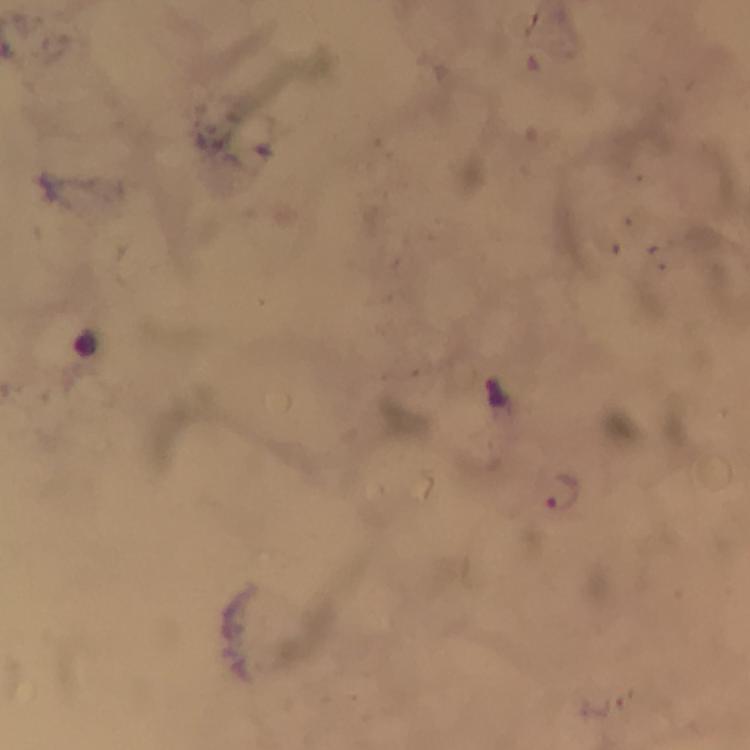

magnification = 100x
malaria parasite locations = approximate centers as (x, y) in pixels: (498, 393), (564, 491)
immersion oil = used
preparation = thick blood film
context = from a malaria diagnostic workup
image size = 750×750 pixels
capture = smartphone camera through the microscope
stain = Giemsa
cropped from = one field of view